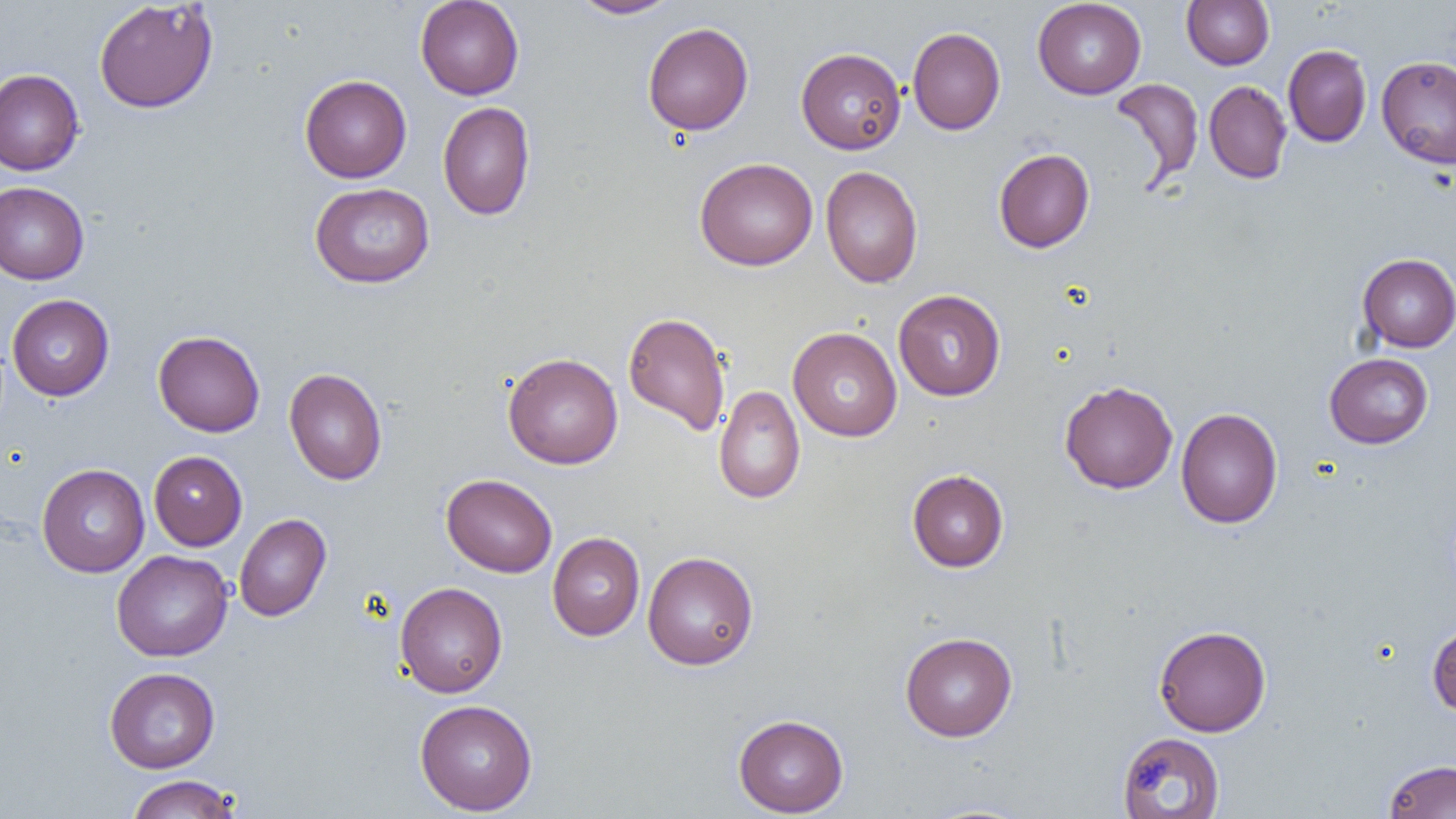

Summary:
  - Coordinate format: approximate bounding boxes as (x1,y1)-(x2,y2) corner pairs in pixels
  - Uninfected red blood cell locations: (415,0)-(524,100), (569,0)-(681,19), (1032,0)-(1146,99), (1181,0)-(1274,70), (93,1)-(219,114), (642,22)-(754,136), (907,27)-(1005,135), (1283,44)-(1371,147), (796,47)-(906,154), (1376,55)-(1456,169), (0,69)-(84,176), (300,75)-(412,183), (1109,77)-(1204,188), (1204,80)-(1292,184), (437,101)-(536,221), (993,148)-(1095,253), (694,157)-(818,271), (821,166)-(923,288), (0,181)-(89,284), (309,183)-(434,288), (1357,253)-(1456,352), (893,289)-(1006,401), (7,294)-(115,401), (623,311)-(731,436), (788,327)-(902,442), (153,330)-(265,437), (503,352)-(623,469), (1324,353)-(1433,448), (284,368)-(387,485), (1059,380)-(1178,494), (713,385)-(805,504), (1176,407)-(1283,528), (149,450)-(247,550), (36,463)-(150,577), (907,469)-(1009,572), (441,473)-(557,577), (234,514)-(331,621), (547,532)-(645,641), (111,549)-(233,662), (642,551)-(759,670), (394,581)-(507,697), (1427,622)-(1456,716), (1153,625)-(1271,736), (900,631)-(1017,741), (104,667)-(220,773), (414,699)-(538,815), (733,714)-(848,817), (1117,731)-(1225,818), (1383,759)-(1456,818), (124,774)-(243,818)
  - Slide-level diagnosis: negative for blood parasites
  - Field of view: single
  - Magnification: 1000x
  - Image size: 1456×819 pixels
  - Modality: optical microscopy
  - Preparation: thin blood film